Identify the blood parasite species.
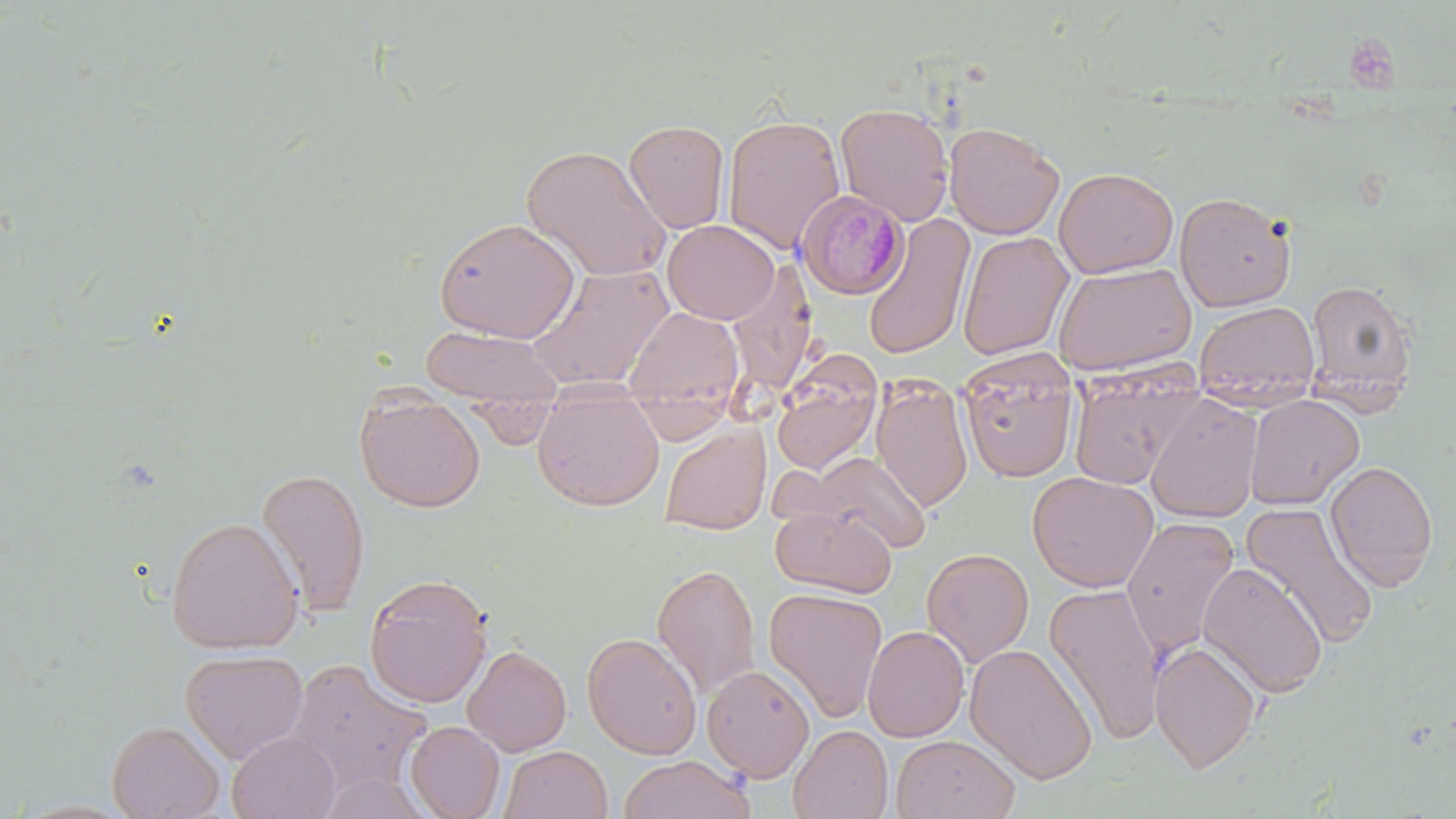
Plasmodium malariae.

Approximate bounding boxes as named x1/y1/x2/y2 corners in pixels. Uninfected red blood cell locations: (x1=835, y1=103, x2=955, y2=226), (x1=722, y1=113, x2=845, y2=254), (x1=624, y1=119, x2=730, y2=234), (x1=944, y1=121, x2=1065, y2=239), (x1=521, y1=144, x2=673, y2=282), (x1=1054, y1=166, x2=1178, y2=278), (x1=1174, y1=190, x2=1297, y2=312), (x1=863, y1=213, x2=975, y2=361), (x1=433, y1=217, x2=580, y2=343), (x1=663, y1=220, x2=780, y2=324), (x1=957, y1=231, x2=1074, y2=361), (x1=732, y1=257, x2=810, y2=391), (x1=526, y1=261, x2=674, y2=393), (x1=1052, y1=261, x2=1197, y2=377), (x1=1305, y1=278, x2=1418, y2=403), (x1=1194, y1=301, x2=1319, y2=410), (x1=623, y1=306, x2=745, y2=421), (x1=421, y1=325, x2=562, y2=411), (x1=957, y1=350, x2=1080, y2=483), (x1=771, y1=359, x2=882, y2=475), (x1=1067, y1=369, x2=1202, y2=489), (x1=871, y1=374, x2=973, y2=513), (x1=532, y1=387, x2=665, y2=511), (x1=355, y1=391, x2=486, y2=512), (x1=1145, y1=393, x2=1264, y2=524), (x1=1244, y1=394, x2=1364, y2=509), (x1=659, y1=423, x2=771, y2=536), (x1=806, y1=451, x2=931, y2=555), (x1=1325, y1=460, x2=1439, y2=591), (x1=256, y1=467, x2=371, y2=617), (x1=1027, y1=470, x2=1159, y2=592), (x1=1240, y1=502, x2=1380, y2=650), (x1=771, y1=506, x2=896, y2=598), (x1=166, y1=516, x2=304, y2=654), (x1=1120, y1=516, x2=1240, y2=659), (x1=921, y1=548, x2=1035, y2=668), (x1=1198, y1=561, x2=1328, y2=697), (x1=652, y1=562, x2=761, y2=698), (x1=364, y1=573, x2=492, y2=708), (x1=1044, y1=582, x2=1165, y2=746), (x1=764, y1=587, x2=888, y2=723), (x1=862, y1=624, x2=969, y2=742), (x1=582, y1=632, x2=703, y2=759), (x1=1150, y1=641, x2=1262, y2=773), (x1=965, y1=643, x2=1098, y2=785), (x1=463, y1=644, x2=572, y2=756), (x1=180, y1=648, x2=310, y2=764), (x1=284, y1=658, x2=432, y2=795), (x1=702, y1=664, x2=815, y2=782), (x1=107, y1=720, x2=226, y2=819), (x1=405, y1=721, x2=505, y2=818), (x1=789, y1=725, x2=892, y2=819), (x1=227, y1=730, x2=341, y2=819), (x1=891, y1=734, x2=1020, y2=818), (x1=499, y1=745, x2=612, y2=819), (x1=618, y1=755, x2=755, y2=819). Platelet locations: (x1=1343, y1=35, x2=1401, y2=92). Plasmodium malariae-infected red blood cell locations: (x1=796, y1=188, x2=909, y2=300). May-Grünwald-Giemsa-stained preparation. 1000x magnification. Optical microscopy. One field of a larger specimen. Image is 1456×819 pixels. Thin blood film.